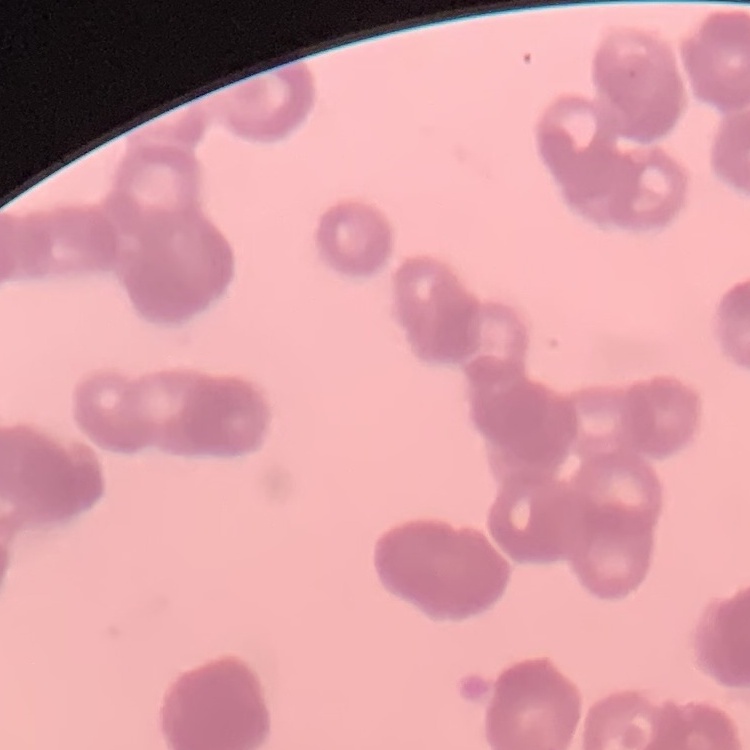 The erythrocytes exhibit rouleaux formation. Thin blood film. Field's or Giemsa stain. One tile cut from a larger photomicrograph.